Describe the morphology of the erythrocytes.
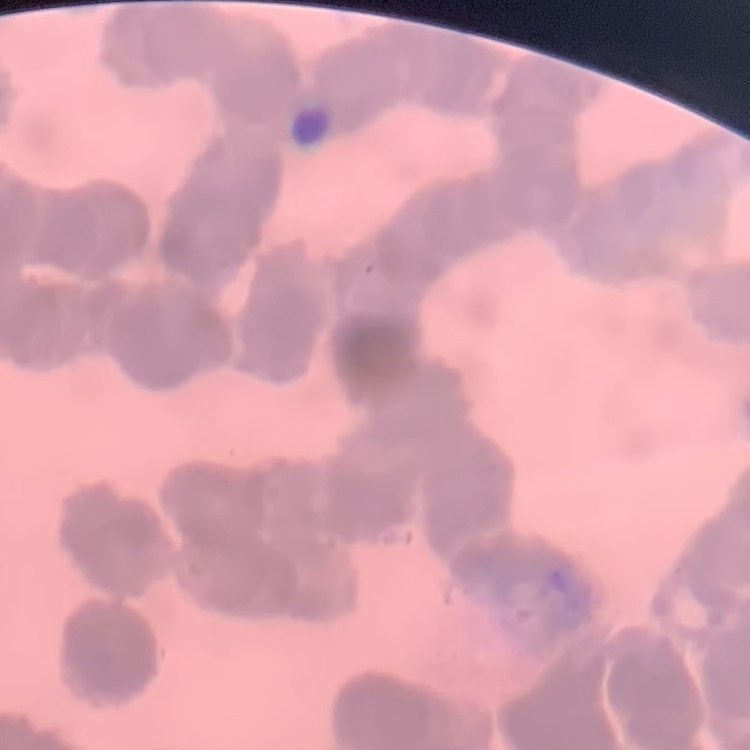

Rouleaux formation.

Stained with either Field's or Giemsa. Thin peripheral smear. One tile cut from a larger photomicrograph.